Classify the preparation.
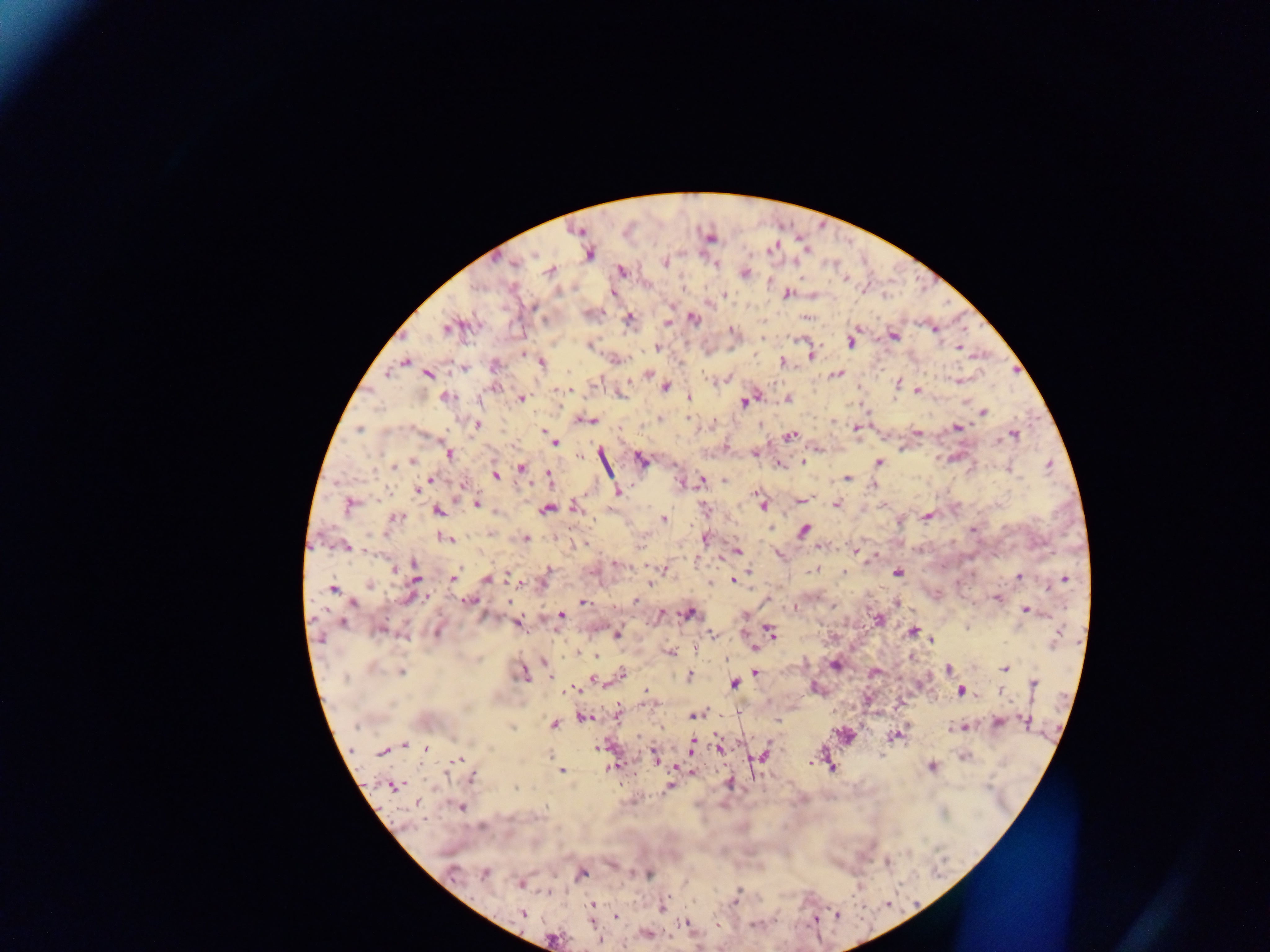

This is a thick smear.

Approximate centers as [x, y] in pixels.
Summary:
  - Plasmodium parasite locations: [577, 231], [709, 237], [589, 252], [665, 262], [514, 263], [716, 264], [551, 271], [621, 271], [743, 272], [613, 293], [787, 293], [725, 295], [628, 318], [692, 318], [669, 323], [448, 327], [933, 328], [732, 332], [893, 335], [762, 337], [851, 340], [589, 344], [655, 347], [958, 347], [522, 353], [811, 355], [615, 359], [780, 361], [404, 362], [541, 363], [495, 365], [464, 368], [387, 371], [428, 373], [647, 373], [835, 373], [727, 379], [958, 380], [897, 384], [496, 386], [665, 386], [568, 390], [917, 391], [688, 396], [445, 397], [788, 398], [521, 399], [744, 401], [983, 412], [661, 418], [584, 419], [476, 423], [957, 427], [359, 428], [855, 428], [917, 433], [1013, 433], [790, 435], [554, 442], [726, 448], [755, 453], [447, 454], [579, 455], [640, 459], [412, 462], [803, 462], [879, 462], [778, 464], [393, 466], [521, 467], [1009, 468], [495, 475], [548, 475], [431, 478], [846, 478], [725, 479], [701, 481], [683, 483], [462, 486], [873, 486], [417, 488], [617, 491], [756, 494], [800, 500], [350, 503], [476, 503], [763, 504], [836, 504], [547, 508], [575, 508], [703, 509], [438, 510], [494, 512], [927, 516], [394, 517], [662, 519], [804, 529], [973, 529], [490, 534], [447, 537], [703, 538], [526, 539], [821, 545], [346, 546], [855, 550], [736, 551], [617, 564], [393, 567], [664, 569], [815, 569], [750, 571], [896, 571], [546, 572], [416, 575], [1018, 576], [453, 577], [487, 578], [1064, 579], [733, 580], [518, 581], [711, 582], [369, 584], [650, 584], [332, 588], [408, 597], [996, 597], [469, 600], [636, 600], [581, 602], [895, 602], [351, 603], [793, 607], [1026, 609], [688, 613], [660, 615], [559, 616], [876, 619], [518, 622], [343, 623], [381, 629], [436, 630], [768, 631], [912, 631], [712, 633], [616, 634], [931, 639], [754, 647], [695, 648], [670, 652], [576, 653], [597, 655], [543, 661], [835, 664], [948, 668], [1004, 668], [400, 671], [755, 671], [522, 672], [874, 672], [620, 675], [689, 675], [550, 679], [593, 679], [733, 683], [1033, 684], [814, 688], [571, 689], [564, 691], [961, 691], [1000, 691], [646, 700], [898, 703], [617, 712], [738, 712], [694, 714], [583, 717], [776, 719], [1025, 720], [996, 722], [554, 724], [961, 727], [895, 736], [403, 746], [692, 746], [599, 747], [426, 748], [718, 748], [383, 750], [654, 756], [756, 756], [762, 756], [964, 756], [461, 758], [612, 766], [676, 766], [932, 766], [832, 767], [560, 770], [692, 771], [471, 778], [729, 783], [393, 785], [668, 786], [417, 803], [460, 806], [885, 861], [612, 864], [484, 872], [647, 873], [451, 874], [581, 874], [518, 883], [591, 905], [661, 907], [523, 914], [836, 916], [615, 917], [815, 917], [685, 923], [646, 933], [552, 939], [599, 940]
  - Country: Ghana
  - Image size: 1270×952 pixels
  - Capture: mobile-phone photograph through a microscope
  - Field of view: single